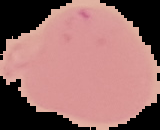

image size = 160×130 pixels
result = negative for Plasmodium parasites
image type = segmented cell region with the area outside set to black
preparation = thin blood film